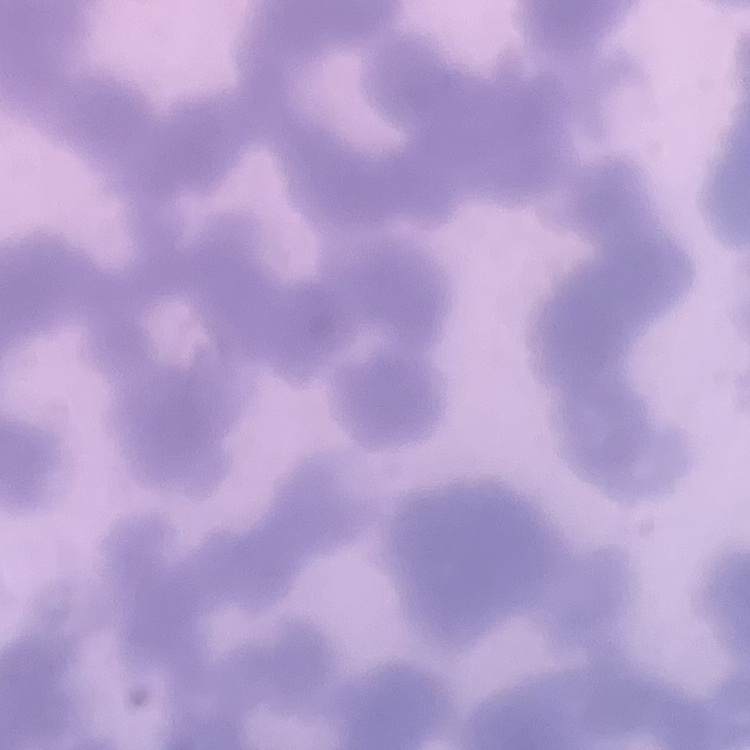
Summary:
  - Erythrocyte morphology: rouleaux formation
  - Preparation: thin blood film
  - Image type: square crop of a larger photomicrograph
  - Stain: Field's or Giemsa